Report the malaria status of this cell.
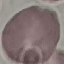
Uninfected.

stain: Giemsa
preparation: thin blood film
capture: smartphone camera at the microscope eyepiece
image_type: cell patch, automatically extracted from a larger field of view and resized to 64 × 64 pixels